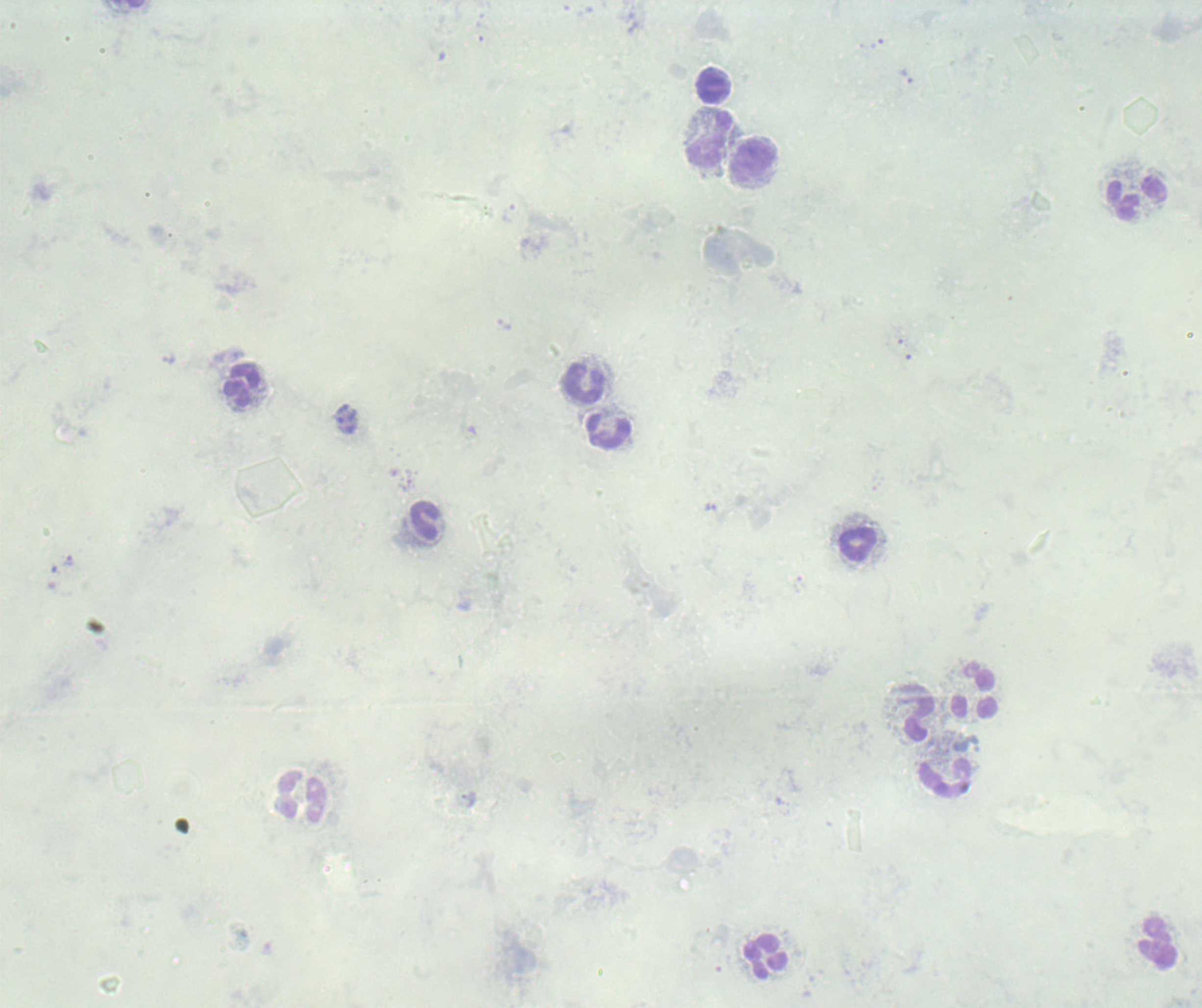
{
  "leukocyte_locations": "approximate centers as [x, y] in pixels: [714, 86], [710, 139], [753, 162], [1137, 199], [585, 384], [242, 385], [609, 431], [424, 521], [858, 545], [975, 694], [916, 712], [944, 778], [301, 797], [1158, 942], [766, 956]",
  "magnification": "100x",
  "preparation": "thick blood smear",
  "context": "previously used in an actual diagnosis",
  "trophozoite_locations": "approximate centers as [x, y] in pixels: [907, 76], [711, 508]",
  "result": "Plasmodium parasites detected",
  "image_size": "1202×1008 pixels",
  "background_quality": "poor",
  "field_of_view": "single",
  "stain": "Romanowsky"
}